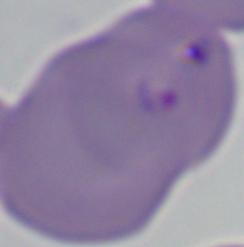

Summary:
  - Identification: Babesia
  - Magnification: 1000x
  - Modality: photomicrograph